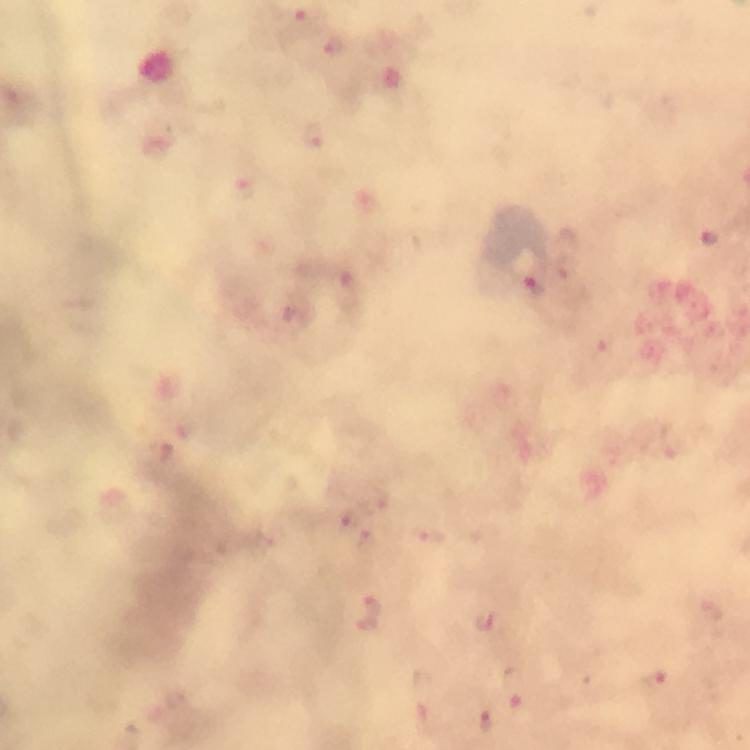
Approximate centers as {x, y} in pixels. Plasmodium parasite locations: {301, 18}, {334, 45}, {312, 135}, {243, 186}, {534, 286}, {348, 293}, {604, 349}, {366, 539}, {714, 608}, {370, 613}, {487, 621}, {654, 680}, {485, 720}. Giemsa stain. Image is 750×750 pixels. A crop from one field of view. At 100x magnification. Immersion oil was used. From a diagnostic examination for malaria. Smartphone photograph taken through a microscope. Thick blood film.